Locate every Plasmodium parasite.
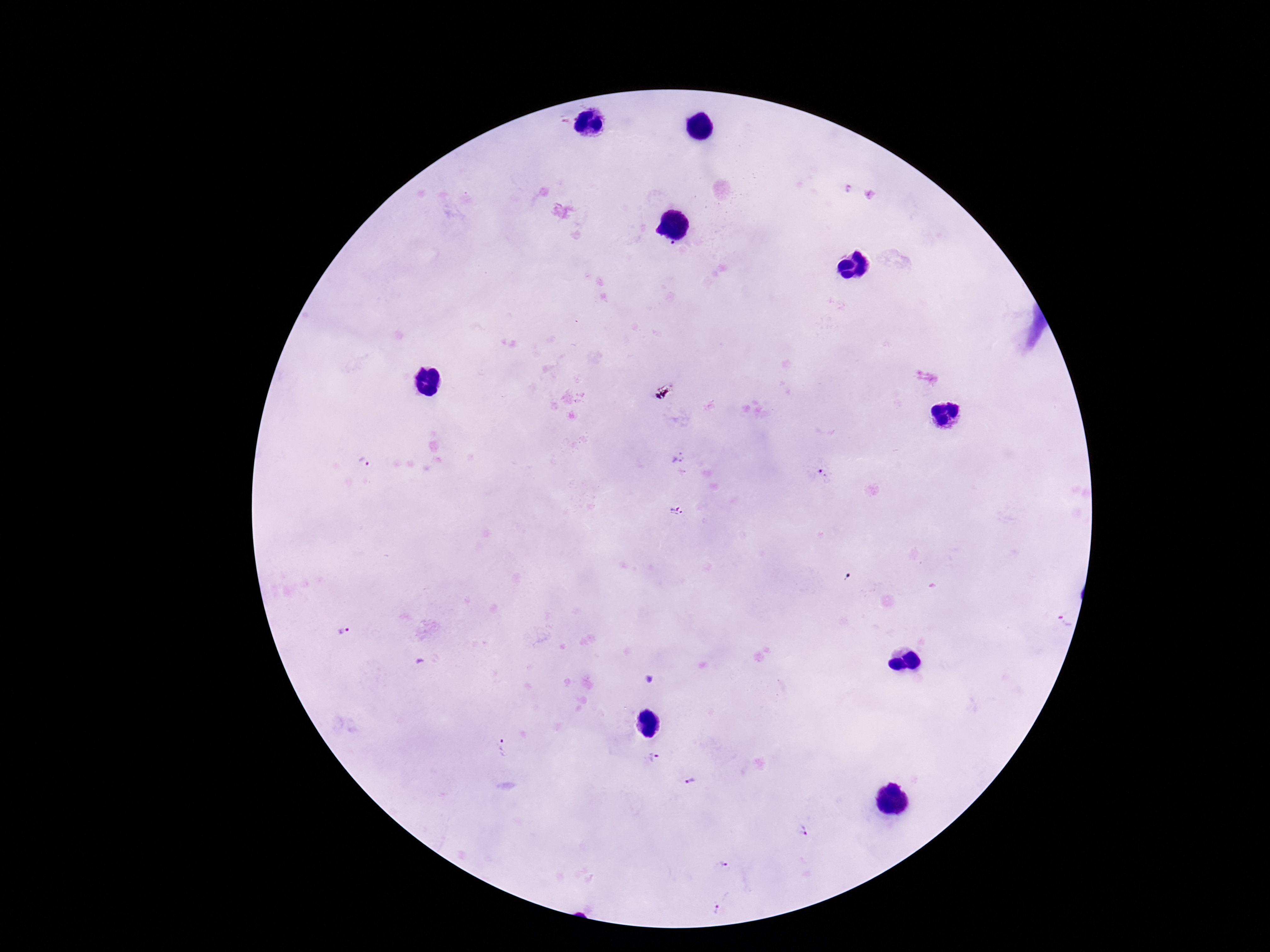

Approximate centers as [x, y] in pixels.
Plasmodium parasites: [848, 190], [677, 457], [365, 463], [820, 470], [676, 512], [1064, 622], [346, 629], [505, 747], [654, 757], [692, 780], [804, 830], [724, 866], [716, 909].

100x magnification. Photographed through the microscope eyepiece with a smartphone camera. Single field of view. Giemsa-stained preparation. Thick peripheral-blood smear. Patient malaria status: positive. Image is 1270×952 pixels.